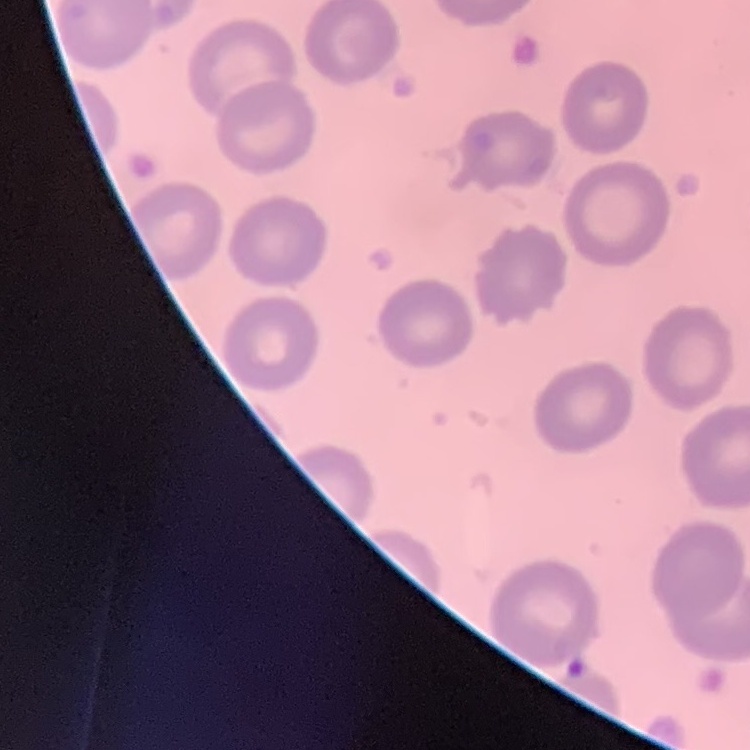 The red blood cells exhibit no rouleaux formation. Field's or Giemsa stain. Thin peripheral smear. One tile cut from a larger photomicrograph.